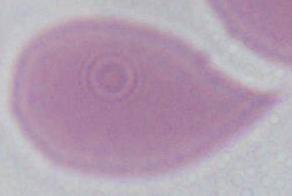

Summary:
  - Modality: micrograph
  - Magnification: 1000x
  - Identification: erythrocyte